Assess this cell for malaria.
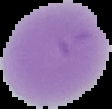
Uninfected.

Summary:
  - Image size: 112×109 pixels
  - Image type: segmented cell region on a black background
  - Preparation: thin blood film